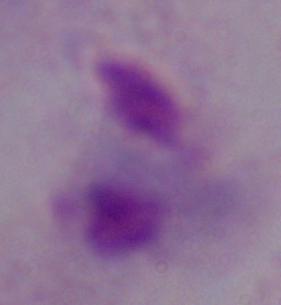

identification = trichomonad
modality = micrograph
magnification = 1000x